Classify this cell by malaria status.
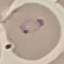

Parasitized.

Photographed with a smartphone camera at the microscope eyepiece. Cell patch, automatically extracted from a larger field of view and resized to 64 × 64 pixels. Thin blood film. Giemsa stain.